Identify the cell.
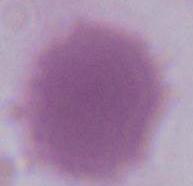

An erythrocyte.

Summary:
  - Magnification: 1000x
  - Modality: micrograph